Report the malaria status of this cell.
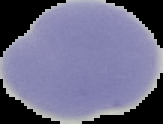
Uninfected.

Summary:
  - Image size: 163×124 pixels
  - Image type: segmented cell region with the area outside set to black
  - Preparation: thin blood film